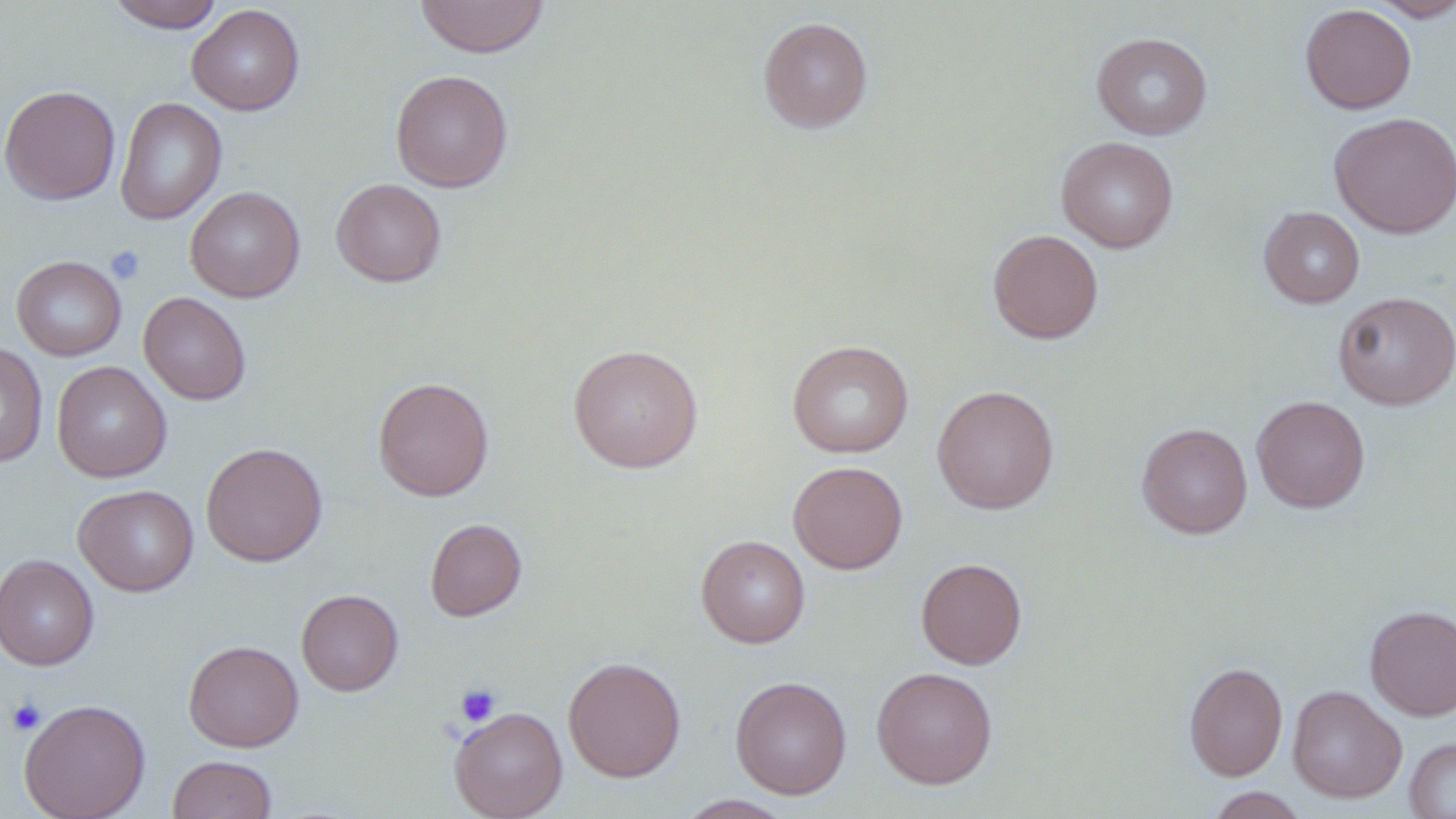

slide-level diagnosis = no evidence of blood parasites
uninfected red blood cell locations = approximate bounding boxes as (x1,y1)-(x2,y2) corner pairs in pixels: (105,0)-(225,32), (414,0)-(550,59), (1369,0)-(1456,22), (187,4)-(305,116), (1300,4)-(1417,114), (757,16)-(873,133), (1091,31)-(1212,140), (390,70)-(513,192), (0,84)-(121,205), (114,97)-(228,225), (1328,111)-(1456,238), (1056,136)-(1179,253), (331,178)-(447,287), (185,186)-(305,303), (1259,206)-(1364,308), (988,229)-(1103,344), (10,255)-(126,361), (139,291)-(251,405), (1334,291)-(1455,409), (786,339)-(914,458), (0,342)-(48,467), (567,343)-(704,473), (51,361)-(172,482), (372,377)-(494,500), (932,385)-(1059,514), (1251,395)-(1370,513), (1137,423)-(1252,538), (201,441)-(328,566), (788,461)-(908,574), (73,484)-(198,596), (425,518)-(527,620), (695,534)-(810,648), (0,553)-(100,670), (916,557)-(1027,670), (296,589)-(403,695), (1365,604)-(1456,720), (184,639)-(304,752), (562,656)-(686,782), (1184,662)-(1288,781), (872,666)-(998,789), (729,675)-(852,799), (1286,685)-(1407,803), (18,698)-(151,819), (449,706)-(567,819), (1404,737)-(1456,818), (167,754)-(277,818), (1203,786)-(1309,818), (673,794)-(797,818)
stain = May-Grünwald-Giemsa
magnification = 1000x
modality = light microscopy
preparation = thin blood film
image size = 1456×819 pixels
platelet locations = approximate bounding boxes as (x1,y1)-(x2,y2) corner pairs in pixels: (106,245)-(146,285), (454,682)-(501,727), (5,697)-(47,736)
field of view = one of a larger specimen